State which cell type is depicted.
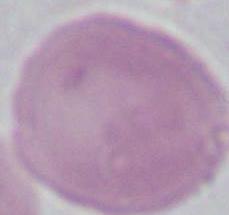
This is an erythrocyte.

Summary:
  - Modality: photomicrograph
  - Magnification: 1000x